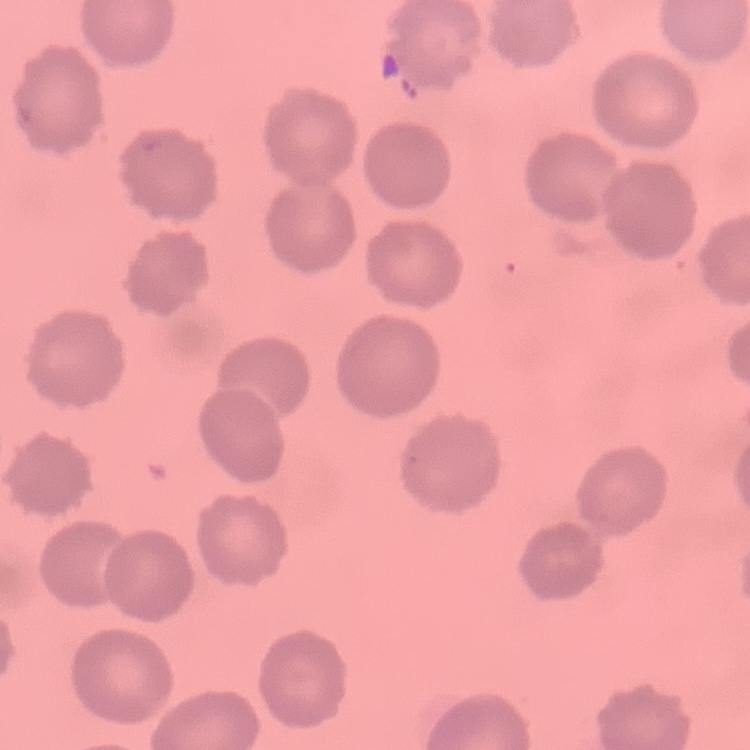
Summary:
  - Red blood cell morphology: no rouleaux formation
  - Image type: square crop of a larger photomicrograph
  - Preparation: thin blood film
  - Stain: Field's or Giemsa